Assess this cell for malaria.
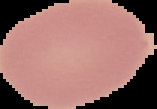
Uninfected.

image type = cell region segmented out of the field of view; surrounding area masked to black
image size = 157×109 pixels
preparation = thin blood film